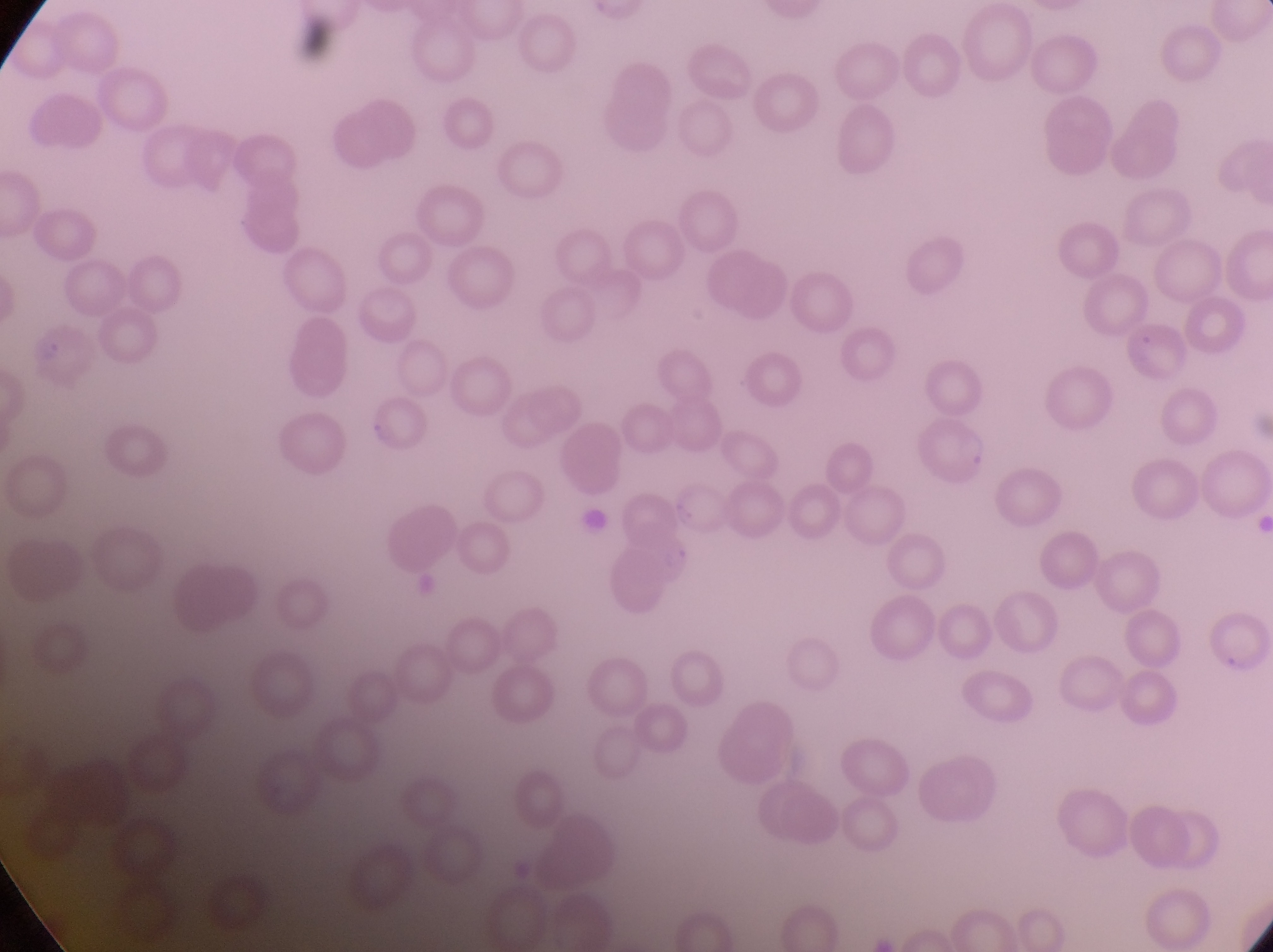
Approximate bounding boxes as {left, top, right, bottom} in pixels.
Summary:
  - Parasitised red blood cell locations: {27, 318, 105, 393}, {366, 397, 435, 454}, {901, 417, 994, 494}
  - Artifact (platelet-like body, stain precipitate, or debris) locations: {577, 502, 609, 541}
  - Country: Uganda
  - Field of view: single
  - Magnification: 1000x
  - Image size: 1273×952 pixels
  - Capture: smartphone photograph through the eyepiece of an Olympus CX-23 microscope
  - Preparation: thin blood film